State the blood parasite species.
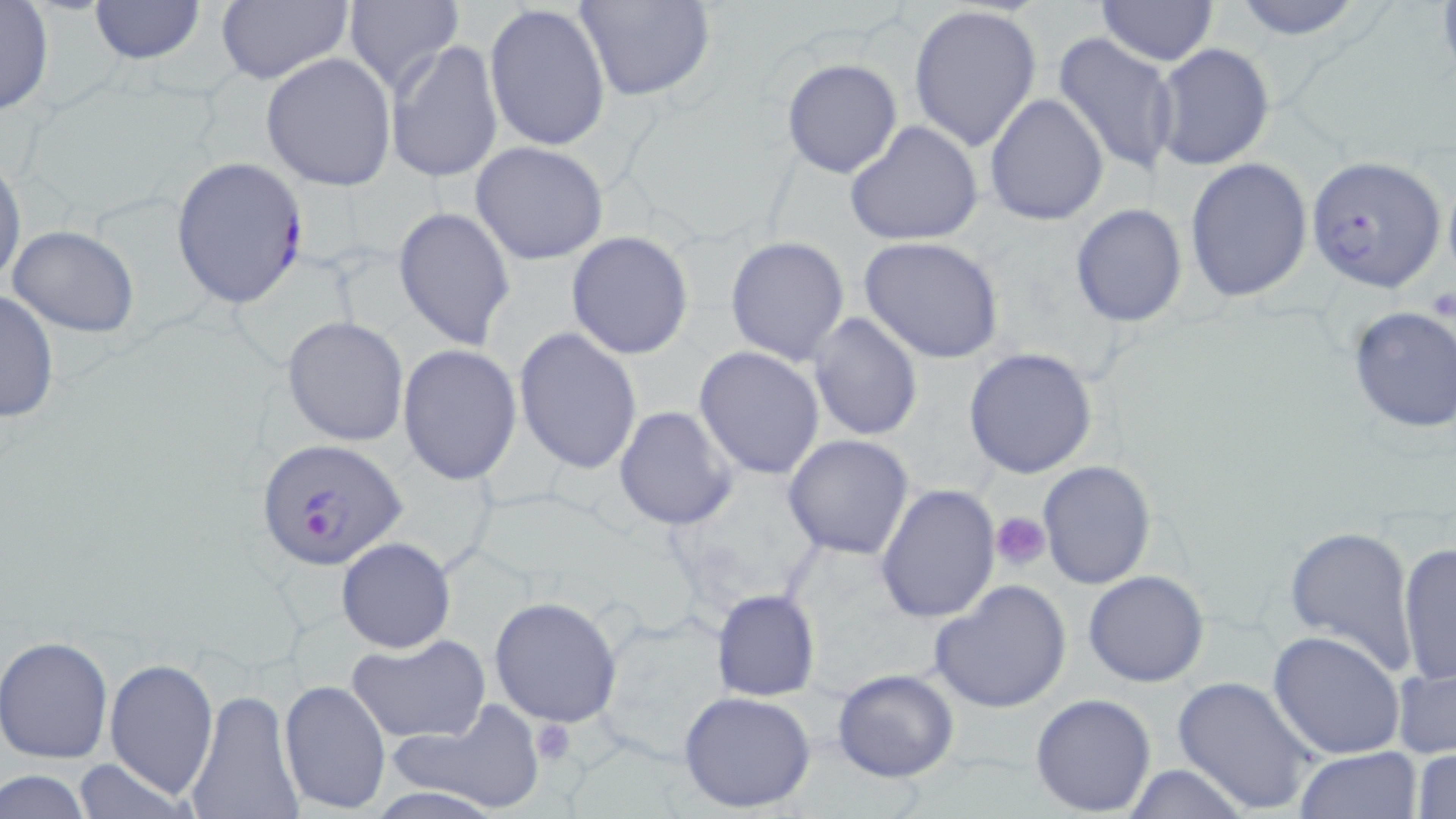
Plasmodium falciparum.

Approximate bounding boxes as named x1/y1/x2/y2 corners in pixels. Plasmodium falciparum-infected red blood cell locations: (x1=1306, y1=153, x2=1447, y2=293), (x1=170, y1=156, x2=309, y2=309), (x1=257, y1=437, x2=408, y2=571). Uninfected red blood cell locations: (x1=0, y1=0, x2=53, y2=116), (x1=89, y1=0, x2=204, y2=63), (x1=215, y1=0, x2=352, y2=85), (x1=578, y1=0, x2=714, y2=101), (x1=1229, y1=0, x2=1366, y2=40), (x1=1096, y1=1, x2=1219, y2=67), (x1=340, y1=2, x2=462, y2=95), (x1=484, y1=3, x2=611, y2=152), (x1=908, y1=4, x2=1041, y2=152), (x1=1053, y1=31, x2=1180, y2=177), (x1=387, y1=39, x2=503, y2=184), (x1=1150, y1=43, x2=1275, y2=173), (x1=260, y1=53, x2=396, y2=191), (x1=780, y1=58, x2=902, y2=179), (x1=986, y1=93, x2=1108, y2=226), (x1=844, y1=120, x2=985, y2=246), (x1=471, y1=141, x2=608, y2=265), (x1=0, y1=156, x2=25, y2=293), (x1=1185, y1=159, x2=1313, y2=304), (x1=1070, y1=201, x2=1187, y2=326), (x1=394, y1=206, x2=515, y2=351), (x1=6, y1=225, x2=139, y2=339), (x1=566, y1=233, x2=693, y2=359), (x1=725, y1=236, x2=850, y2=365), (x1=859, y1=236, x2=1005, y2=363), (x1=0, y1=288, x2=58, y2=424), (x1=1346, y1=307, x2=1456, y2=433), (x1=807, y1=311, x2=923, y2=443), (x1=282, y1=315, x2=409, y2=446), (x1=514, y1=327, x2=642, y2=475), (x1=397, y1=343, x2=522, y2=484), (x1=694, y1=347, x2=825, y2=480), (x1=963, y1=347, x2=1098, y2=479), (x1=614, y1=405, x2=740, y2=531), (x1=782, y1=434, x2=915, y2=559), (x1=1036, y1=460, x2=1157, y2=590), (x1=876, y1=484, x2=1001, y2=626), (x1=1282, y1=524, x2=1419, y2=677), (x1=336, y1=537, x2=456, y2=653), (x1=1396, y1=543, x2=1455, y2=687), (x1=1083, y1=569, x2=1208, y2=686), (x1=928, y1=580, x2=1073, y2=714), (x1=711, y1=588, x2=820, y2=702), (x1=489, y1=597, x2=622, y2=727), (x1=1267, y1=629, x2=1408, y2=759), (x1=347, y1=634, x2=489, y2=743), (x1=1, y1=636, x2=113, y2=764), (x1=103, y1=658, x2=218, y2=799), (x1=1390, y1=662, x2=1455, y2=762), (x1=832, y1=668, x2=959, y2=783), (x1=1172, y1=674, x2=1319, y2=815), (x1=278, y1=678, x2=391, y2=816), (x1=678, y1=689, x2=817, y2=814), (x1=184, y1=690, x2=303, y2=819), (x1=1030, y1=693, x2=1157, y2=817), (x1=385, y1=703, x2=545, y2=813), (x1=1410, y1=745, x2=1456, y2=819), (x1=1294, y1=746, x2=1423, y2=819), (x1=69, y1=758, x2=195, y2=819), (x1=1118, y1=763, x2=1250, y2=819), (x1=1, y1=769, x2=96, y2=819). Platelet locations: (x1=990, y1=511, x2=1051, y2=571), (x1=528, y1=718, x2=577, y2=764). Captured at 1000x magnification. May-Grünwald-Giemsa stain. Thin blood smear. Single field of view. Light microscopy. Image is 1456×819 pixels.